Locate the cells, classifying each as a parasitized red blood cell, an uninfected red blood cell, or a white blood cell.
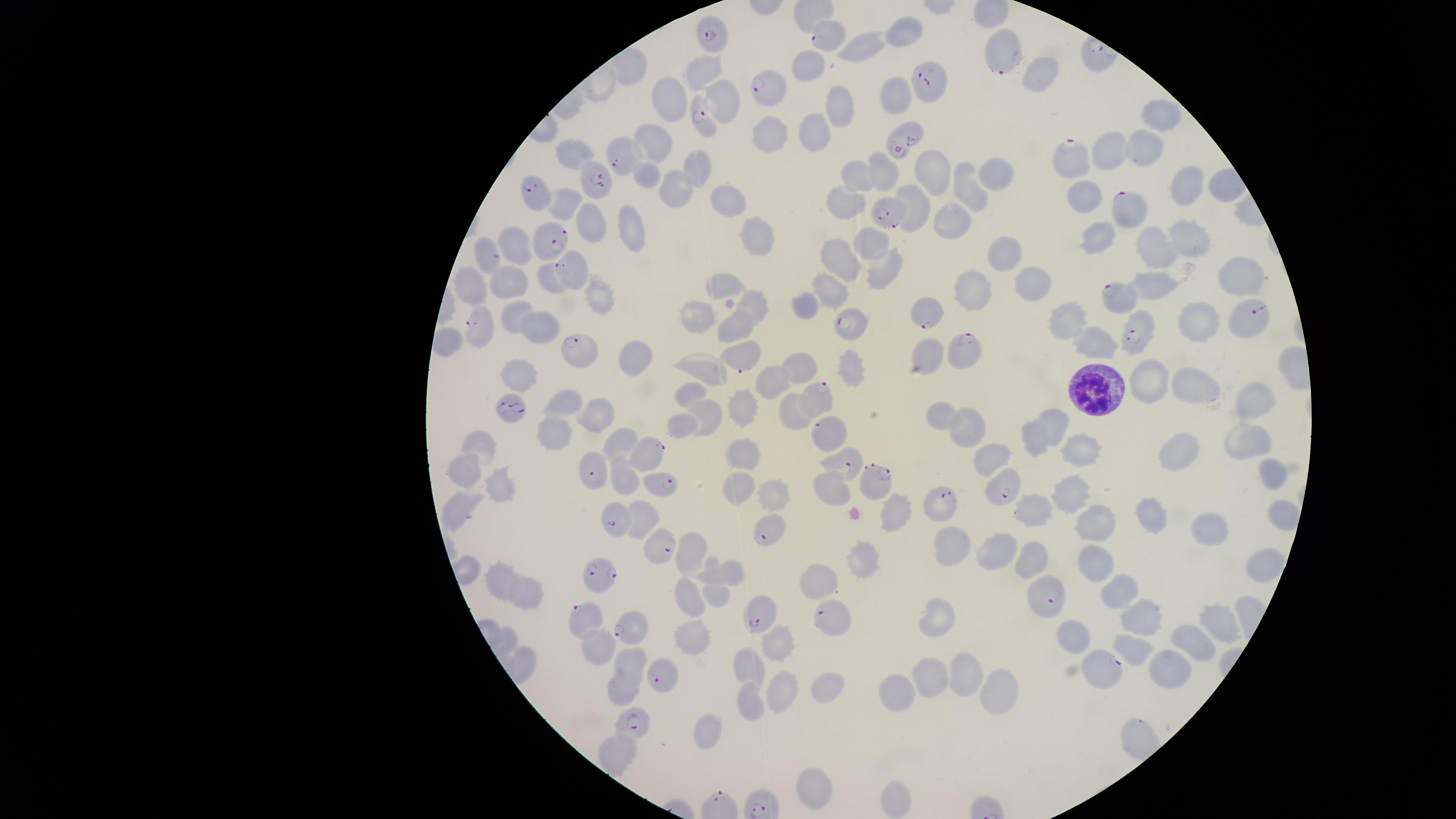
Approximate marker points, in pixels from the top-left corner.
Parasitized red blood cells: (x=713, y=32), (x=824, y=32), (x=1001, y=59), (x=931, y=81), (x=764, y=86), (x=700, y=115), (x=899, y=136), (x=1072, y=157), (x=626, y=159), (x=591, y=180), (x=543, y=197), (x=891, y=211), (x=1125, y=211), (x=549, y=239), (x=567, y=268), (x=1113, y=300), (x=927, y=312), (x=852, y=320), (x=1246, y=322), (x=480, y=327), (x=1138, y=331), (x=574, y=344), (x=966, y=353), (x=746, y=359), (x=814, y=398), (x=510, y=409), (x=825, y=429), (x=647, y=450), (x=848, y=458), (x=590, y=469), (x=663, y=483), (x=877, y=486), (x=1009, y=489), (x=945, y=502), (x=619, y=519), (x=770, y=525), (x=662, y=546), (x=598, y=570), (x=1046, y=597), (x=757, y=617), (x=829, y=619), (x=587, y=621), (x=631, y=623), (x=1103, y=665), (x=662, y=673), (x=633, y=722).
Uninfected red blood cells: (x=899, y=33), (x=862, y=46), (x=810, y=62), (x=701, y=67), (x=1041, y=70), (x=671, y=92), (x=893, y=92), (x=722, y=96), (x=839, y=107), (x=1161, y=118), (x=777, y=128), (x=815, y=131), (x=657, y=136), (x=1145, y=145), (x=571, y=150), (x=1114, y=150), (x=695, y=167), (x=884, y=169), (x=935, y=170), (x=648, y=174), (x=995, y=174), (x=856, y=175), (x=1186, y=185), (x=970, y=189), (x=676, y=191), (x=911, y=194), (x=1084, y=197), (x=720, y=199), (x=848, y=204), (x=565, y=205), (x=950, y=215), (x=591, y=221), (x=636, y=223), (x=753, y=231), (x=1184, y=234), (x=1096, y=236), (x=874, y=242), (x=512, y=247), (x=1153, y=248), (x=1005, y=253), (x=844, y=255), (x=485, y=256), (x=888, y=266), (x=1234, y=272), (x=508, y=278), (x=547, y=278), (x=1157, y=283), (x=1028, y=284), (x=719, y=285), (x=833, y=287), (x=475, y=288), (x=972, y=288), (x=599, y=298), (x=812, y=300), (x=757, y=306), (x=518, y=308), (x=1198, y=314), (x=699, y=317), (x=1072, y=318), (x=536, y=326), (x=740, y=326), (x=1100, y=344), (x=931, y=350), (x=630, y=353), (x=802, y=364), (x=846, y=365), (x=708, y=370), (x=525, y=373), (x=776, y=378), (x=1148, y=379), (x=1192, y=379), (x=690, y=392), (x=1251, y=397), (x=570, y=399), (x=740, y=406), (x=601, y=410), (x=795, y=410), (x=942, y=414), (x=707, y=415), (x=1056, y=420), (x=965, y=427), (x=685, y=428), (x=562, y=433), (x=1033, y=433), (x=1249, y=433), (x=621, y=440), (x=478, y=445), (x=1179, y=445), (x=1088, y=449), (x=747, y=455), (x=990, y=457), (x=466, y=465), (x=1265, y=474), (x=627, y=477), (x=502, y=485), (x=739, y=487), (x=1068, y=487), (x=829, y=489), (x=776, y=493), (x=462, y=507), (x=893, y=511), (x=1039, y=512), (x=1276, y=513), (x=1154, y=515), (x=1096, y=523), (x=1213, y=532), (x=951, y=545), (x=987, y=547), (x=696, y=551), (x=1037, y=556), (x=864, y=559), (x=1089, y=559), (x=728, y=567), (x=1258, y=567), (x=499, y=572), (x=821, y=582), (x=1117, y=588), (x=529, y=593), (x=684, y=596), (x=710, y=596), (x=1141, y=612), (x=938, y=618), (x=1214, y=618), (x=1069, y=634), (x=693, y=638), (x=1193, y=642), (x=776, y=646), (x=598, y=648), (x=1138, y=649), (x=629, y=660), (x=1174, y=665), (x=748, y=666), (x=971, y=671), (x=936, y=675), (x=830, y=684), (x=1001, y=690), (x=899, y=691), (x=621, y=692), (x=777, y=694), (x=752, y=705), (x=708, y=732), (x=614, y=756), (x=811, y=780), (x=895, y=797).
White blood cells: (x=1090, y=388).

field of view = single
visible region = circular
species = Plasmodium falciparum
preparation = thin smear of blood
stain = Giemsa
capture = smartphone photograph through the microscope eyepiece
image size = 1456×819 pixels